Assess this cell for malaria.
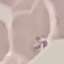
It is parasitized.

Acquired by smartphone through the microscope eyepiece. Giemsa-stained preparation. Thin smear of blood. Cell patch, automatically extracted from a larger field of view and resized to 64 × 64 pixels.